Point out malaria parasites and leukocytes.
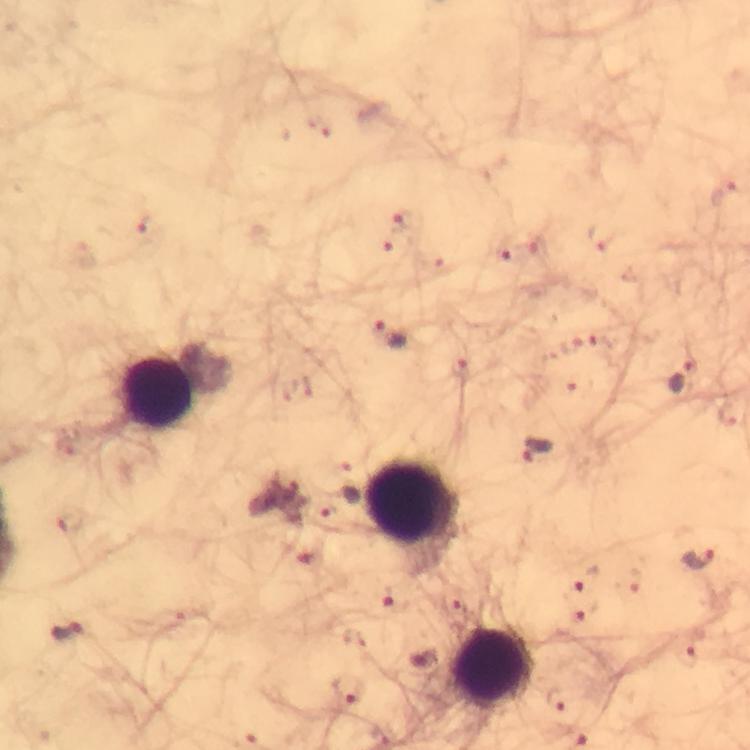

Approximate object centers, in pixels from the top-left corner.
Malaria parasites: (x=725, y=194), (x=399, y=220), (x=148, y=227), (x=602, y=235), (x=539, y=246), (x=505, y=253), (x=388, y=333), (x=460, y=367), (x=686, y=380), (x=537, y=451), (x=340, y=501), (x=698, y=559), (x=585, y=577), (x=396, y=599), (x=586, y=611), (x=70, y=632), (x=688, y=653), (x=347, y=688), (x=557, y=698).
Leukocytes: (x=157, y=392), (x=409, y=507), (x=490, y=666).

Immersion oil was used. Thick smear. 100x magnification. Giemsa-stained preparation. Photographed through the microscope with a smartphone camera. Image is 750×750 pixels. Cropped region of a single field of view. From a diagnostic examination for malaria.